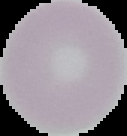 Malaria status: uninfected. Image is 127×136 pixels. From a thin blood film. Segmented cell region on a black background.